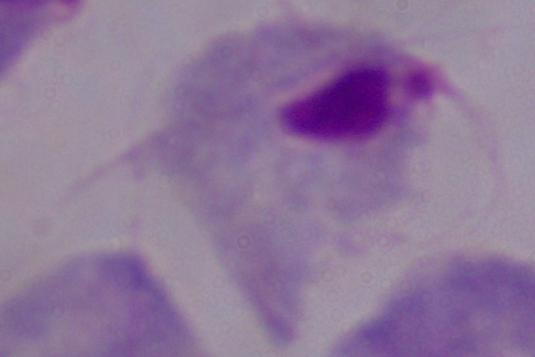
Micrograph. A trichomonad is seen. Captured at 1000x magnification.